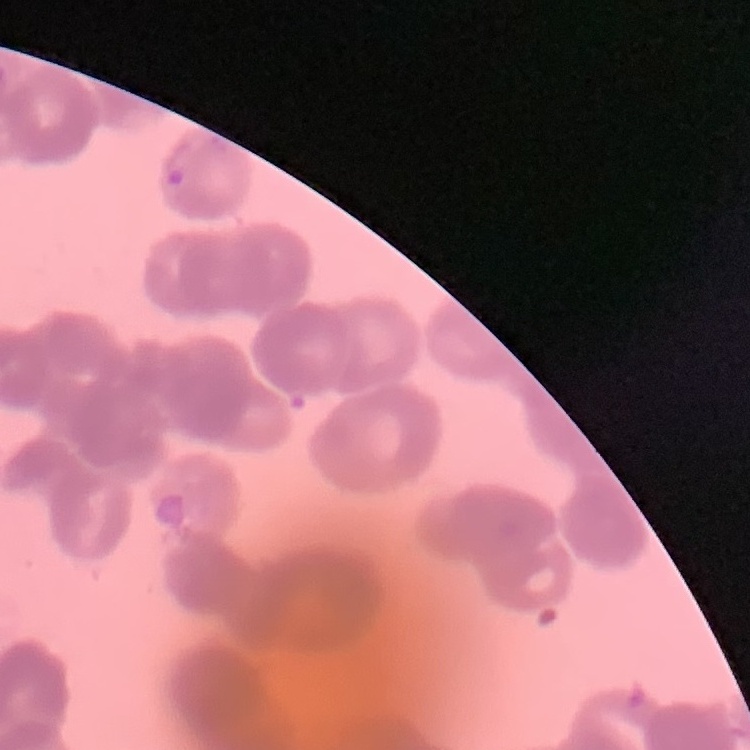

Summary:
  - Erythrocyte morphology: rouleaux formation
  - Image type: one tile cut from a larger photomicrograph
  - Stain: Field's or Giemsa
  - Preparation: thin blood smear